Comment on the morphology of the erythrocytes.
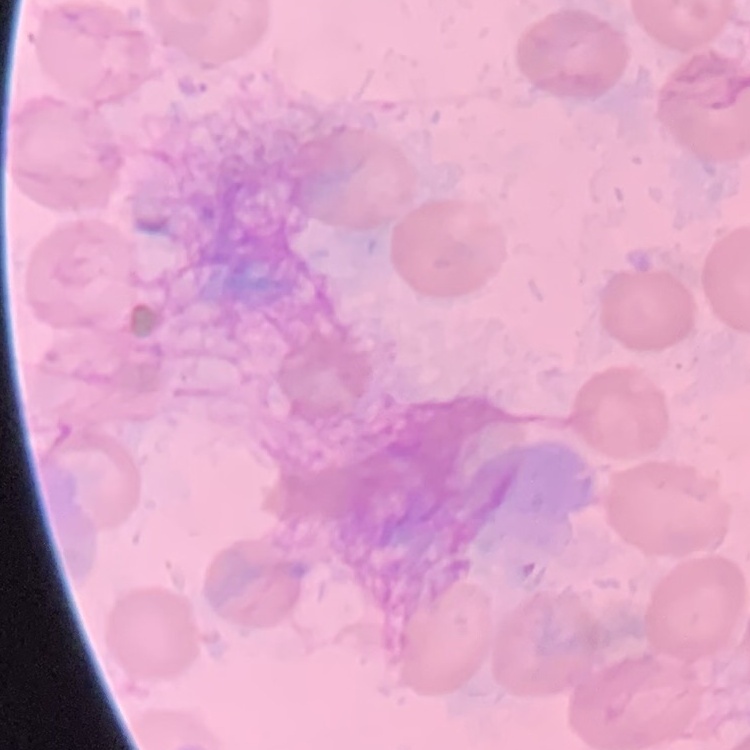

No rouleaux formation.

Square crop of a larger photomicrograph. Thin peripheral smear. Field's or Giemsa stain.